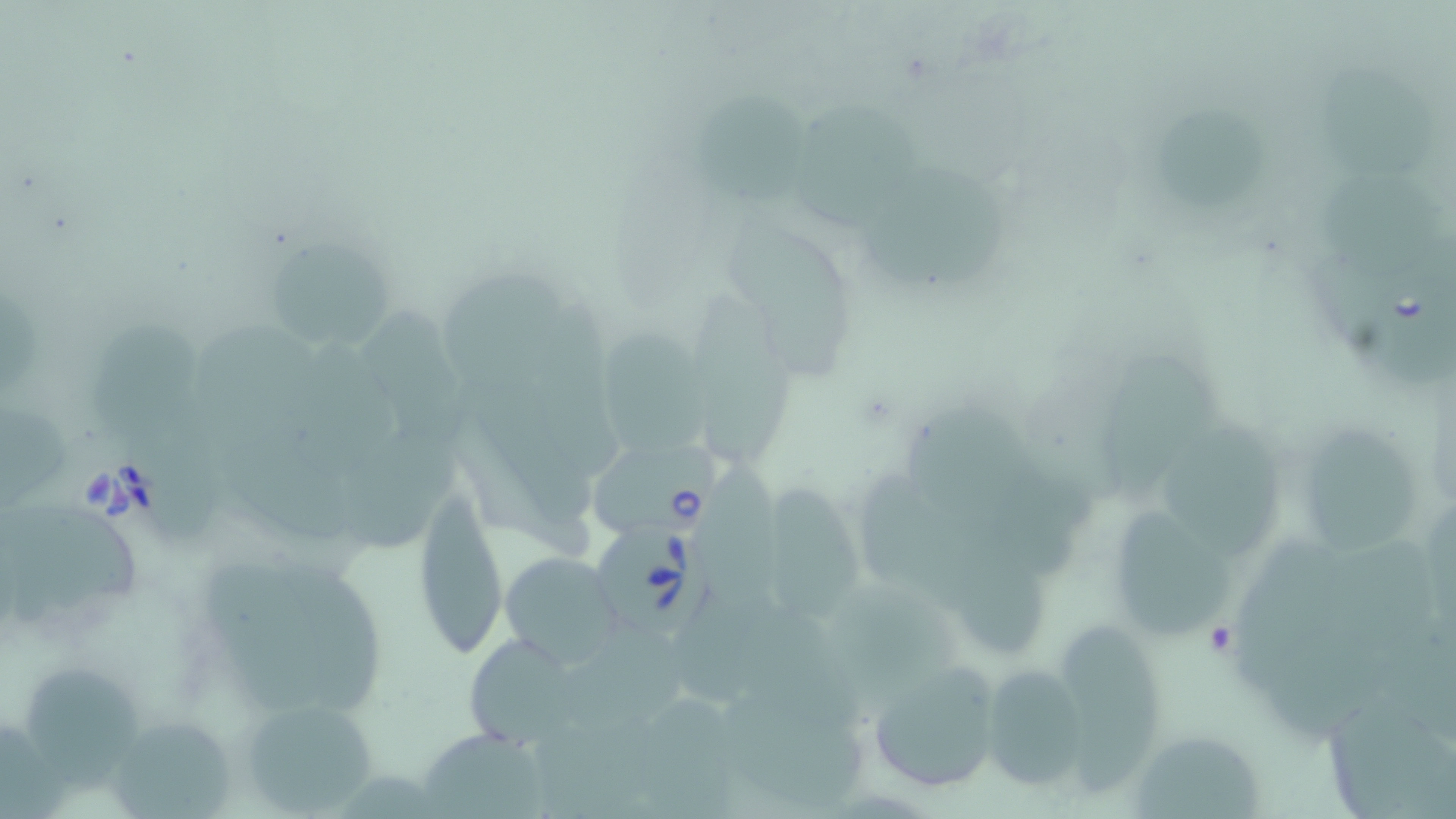
slide-level diagnosis = Babesia divergens
image size = 1456×819 pixels
magnification = 1000x
uninfected red blood cell locations = approximate bounding boxes as (x1, y1, x2, y2) in pixels: (1317, 61, 1436, 185), (699, 92, 808, 206), (793, 95, 922, 229), (1161, 104, 1273, 215), (859, 167, 1011, 284), (1318, 168, 1451, 278), (721, 216, 861, 377), (263, 243, 391, 352), (433, 266, 573, 387), (696, 301, 802, 467), (82, 322, 199, 441), (596, 323, 710, 452), (1108, 354, 1219, 496), (903, 399, 1031, 511), (0, 401, 70, 511), (1163, 415, 1283, 557), (1302, 419, 1420, 559), (347, 425, 464, 542), (226, 431, 377, 548), (706, 468, 791, 607), (864, 475, 979, 605), (772, 488, 862, 619), (412, 491, 509, 659), (14, 500, 142, 614), (1119, 504, 1233, 641), (945, 517, 1052, 659), (498, 551, 624, 667), (209, 565, 329, 714), (288, 568, 388, 714), (832, 583, 955, 708), (682, 594, 775, 701), (740, 605, 870, 738), (1061, 623, 1162, 793), (572, 633, 698, 742), (1268, 633, 1402, 740), (462, 636, 584, 743), (864, 658, 1006, 796), (979, 660, 1095, 793), (18, 665, 139, 793), (238, 696, 382, 816), (726, 696, 872, 808), (1323, 697, 1455, 819), (108, 713, 235, 819), (422, 732, 556, 818), (1138, 733, 1262, 819)
stain = May-Grünwald-Giemsa
modality = light microscopy
Babesia divergens-infected red blood cell locations = approximate bounding boxes as (x1, y1, x2, y2) in pixels: (1369, 241, 1455, 384), (589, 439, 726, 539), (593, 518, 720, 637)
field of view = one of a larger specimen
preparation = thin blood smear